Assess this cell for malaria.
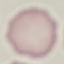
Uninfected.

capture = smartphone camera at the microscope eyepiece
image type = cell patch, automatically extracted from a larger field of view and resized to 64 × 64 pixels
preparation = thin smear
stain = Giemsa